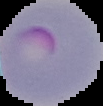

{
  "image_size": "103×106 pixels",
  "image_type": "cell region segmented out of the field of view; surrounding area masked to black",
  "preparation": "thin blood film",
  "result": "malaria parasites detected"
}